Point out each leukocyte.
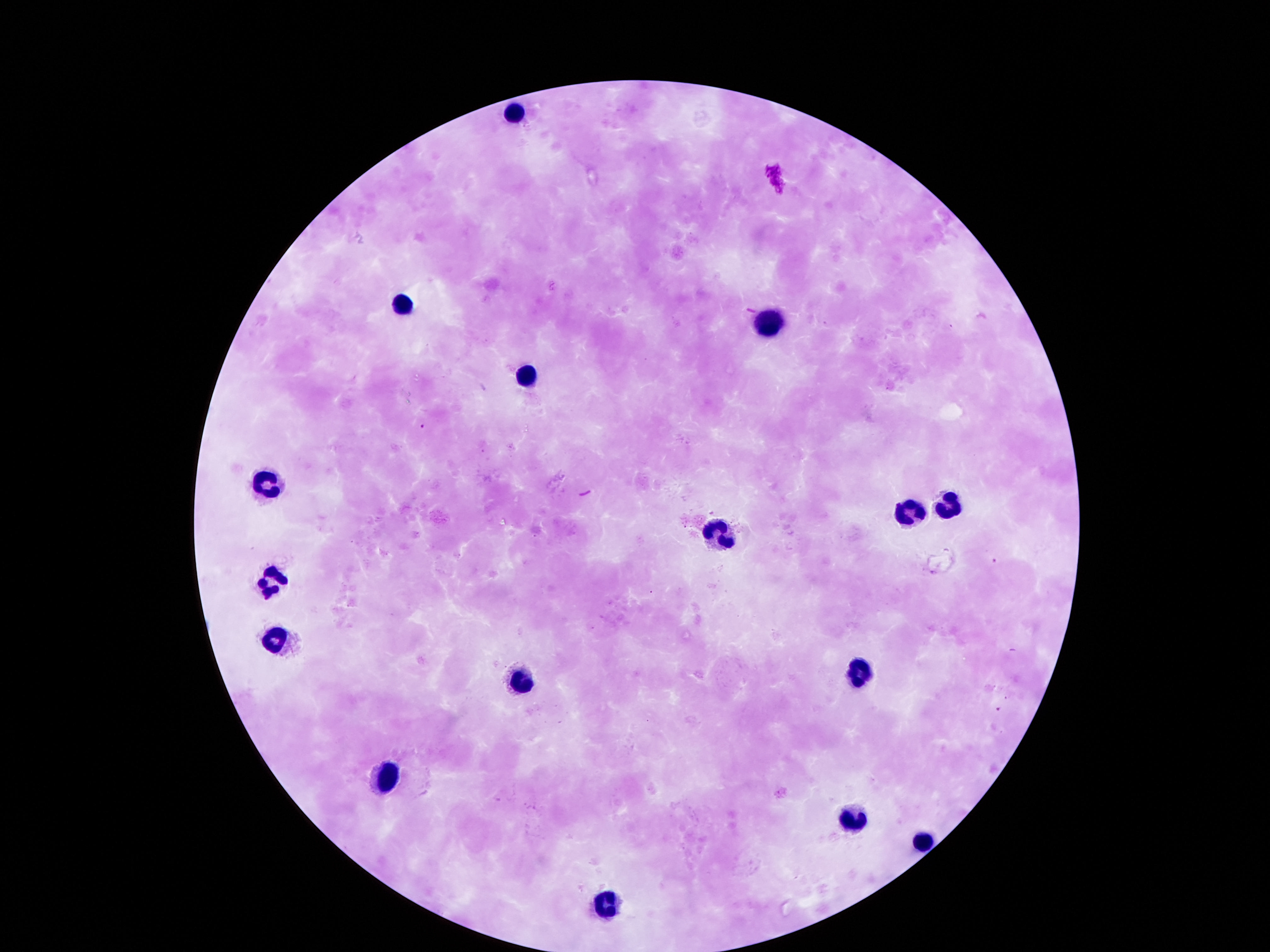

Approximate centers as {x, y} in pixels.
Leukocytes: {514, 110}, {403, 301}, {766, 320}, {528, 375}, {266, 483}, {948, 503}, {904, 512}, {719, 532}, {266, 580}, {276, 633}, {861, 673}, {521, 684}, {387, 782}, {857, 814}, {918, 838}, {608, 903}.

{
  "magnification": "100x",
  "patient_malaria_status": "not infected",
  "image_size": "1270×952 pixels",
  "field_of_view": "one from this slide",
  "preparation": "thick peripheral-blood smear",
  "capture": "smartphone camera through the microscope eyepiece",
  "stain": "Giemsa"
}